Locate and identify every blood parasite.
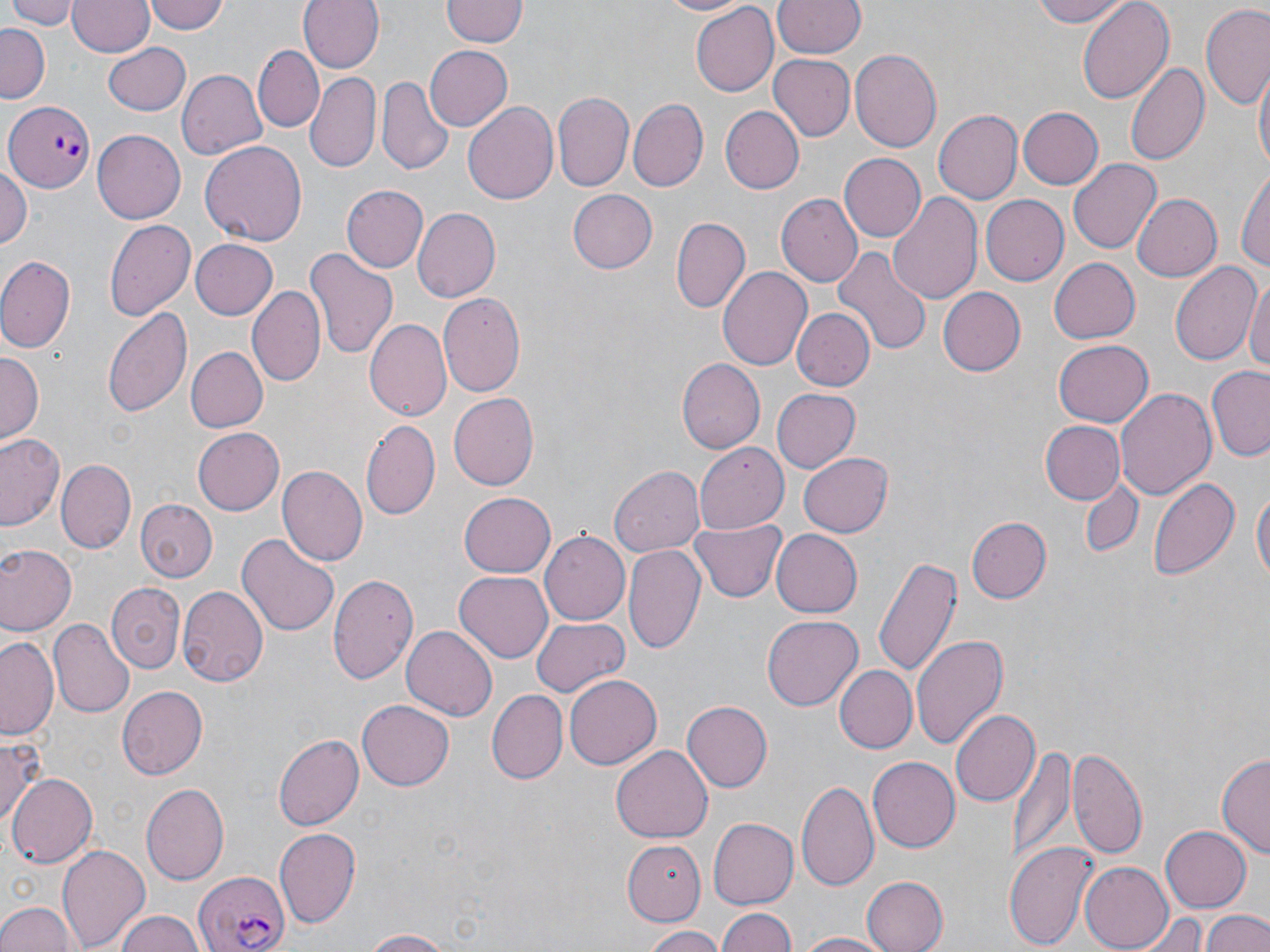
Approximate bounding boxes as (x1,y1)-(x2,y2) corner pairs in pixels.
Plasmodium falciparum-infected red blood cells: (5,99)-(93,193), (195,871)-(289,952).
No Plasmodium ovale, Plasmodium malariae, Plasmodium vivax, Babesia divergens, or Trypanosoma brucei observed.

Uninfected red blood cell locations: (6,0)-(79,29), (148,0)-(229,36), (298,0)-(383,74), (654,0)-(755,17), (772,0)-(865,59), (1025,0)-(1133,28), (1076,0)-(1175,106), (68,1)-(154,58), (441,2)-(526,47), (691,4)-(778,95), (1200,6)-(1270,109), (0,23)-(50,101), (104,42)-(192,115), (255,45)-(325,132), (423,45)-(512,132), (850,48)-(943,153), (769,55)-(856,140), (1125,60)-(1209,168), (1253,67)-(1268,177), (176,69)-(267,160), (304,74)-(380,174), (376,78)-(452,175), (553,90)-(634,192), (630,98)-(707,191), (463,100)-(559,206), (721,105)-(805,194), (1016,106)-(1103,191), (932,108)-(1021,201), (92,130)-(185,224), (200,140)-(307,243), (838,153)-(926,243), (1069,158)-(1161,253), (0,165)-(31,250), (1236,166)-(1270,276), (342,184)-(429,274), (565,189)-(657,274), (888,190)-(983,306), (775,193)-(862,286), (979,196)-(1067,286), (1134,196)-(1221,281), (410,208)-(497,301), (672,217)-(749,313), (103,218)-(196,322), (189,240)-(277,319), (833,245)-(932,356), (305,248)-(399,359), (0,255)-(76,353), (1049,259)-(1140,343), (1169,260)-(1260,368), (717,266)-(812,368), (1246,276)-(1270,380), (249,284)-(324,387), (938,288)-(1025,376), (438,292)-(526,398), (102,305)-(194,418), (790,307)-(874,392), (364,317)-(451,421), (1054,340)-(1152,426), (185,346)-(268,433), (0,350)-(43,438), (676,359)-(765,455), (1206,367)-(1270,463), (771,386)-(860,472), (1116,387)-(1216,501), (448,392)-(539,490), (360,416)-(440,520), (1041,420)-(1123,503), (194,427)-(285,515), (0,431)-(67,533), (694,443)-(787,532), (799,452)-(893,537), (57,460)-(135,553), (278,465)-(368,568), (610,465)-(705,556), (1147,473)-(1240,582), (1075,477)-(1146,559), (1251,481)-(1268,596), (456,491)-(556,578), (136,500)-(217,581), (965,516)-(1052,604), (688,519)-(787,605), (771,529)-(862,617), (539,530)-(630,624), (237,533)-(338,639), (2,543)-(75,633), (623,545)-(705,656), (874,555)-(959,679), (454,572)-(553,663), (328,573)-(419,687), (108,583)-(184,673), (177,584)-(272,688), (763,615)-(864,710), (531,616)-(629,698), (48,618)-(134,717), (402,625)-(497,721), (911,634)-(1008,753), (1,635)-(61,742), (837,665)-(917,752), (564,675)-(659,770), (117,686)-(207,779), (487,690)-(567,784), (358,697)-(453,787), (683,701)-(773,790), (949,709)-(1038,808), (275,733)-(363,830), (0,735)-(46,830), (611,743)-(711,844), (1009,744)-(1074,869), (1068,746)-(1149,863), (1218,750)-(1270,860), (866,756)-(960,853), (8,773)-(97,870), (796,778)-(880,893), (140,783)-(229,886), (709,819)-(797,905), (1158,825)-(1251,912), (274,828)-(360,925), (624,838)-(707,924), (1007,839)-(1100,952), (58,843)-(151,952), (1079,862)-(1173,949), (858,875)-(947,952), (0,900)-(79,952), (716,906)-(796,952), (112,909)-(207,952), (1200,909)-(1270,952), (1133,910)-(1213,952), (638,926)-(724,952), (357,929)-(459,951), (795,932)-(893,951). Slide-level diagnosis: Plasmodium falciparum. One field of a larger specimen. Image is 1270×952 pixels. May-Grünwald-Giemsa stain. Optical microscopy. Thin blood smear. Captured at 1000x magnification.